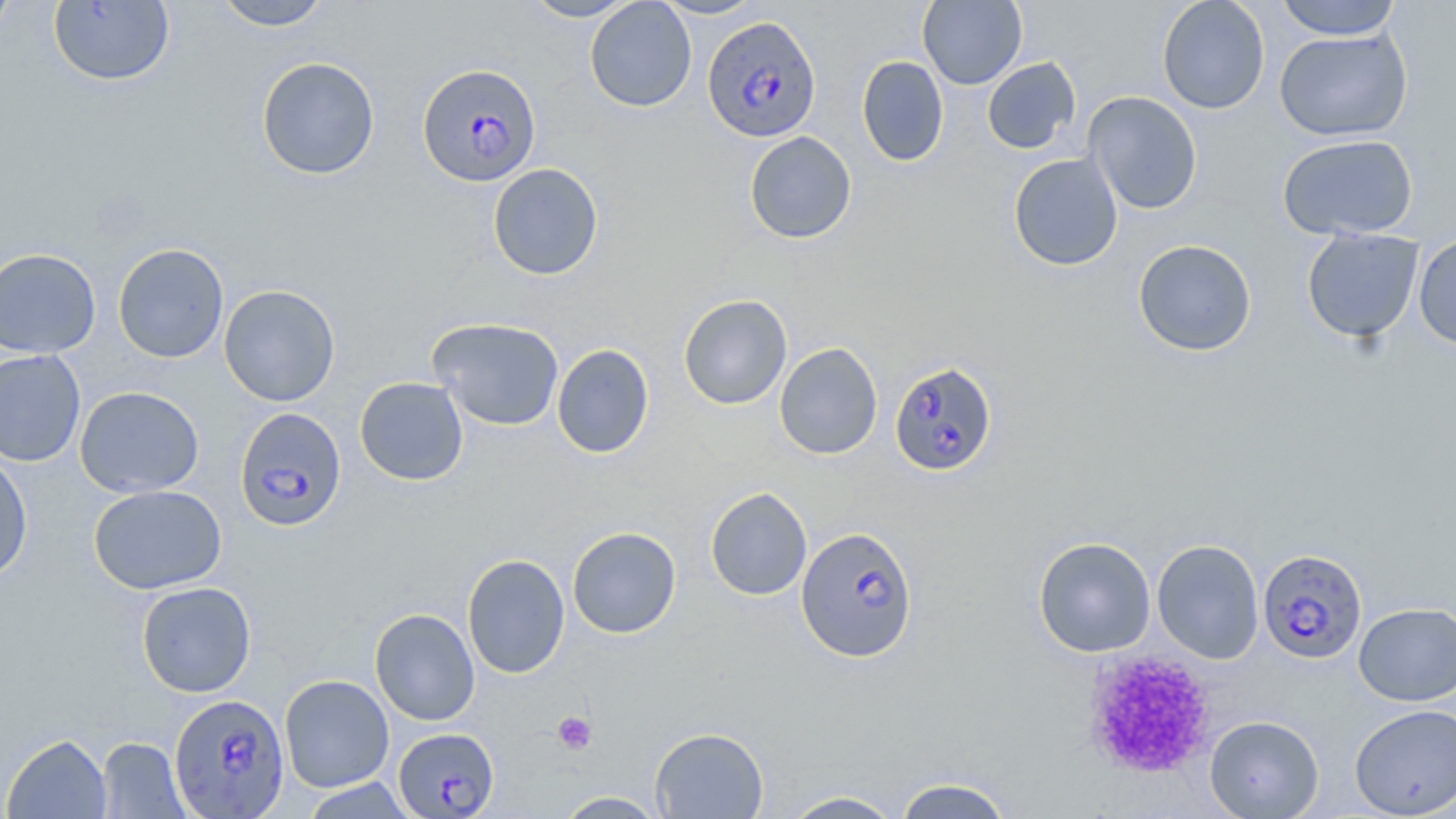
Summary:
  - Coordinate format: approximate bounding boxes as (x1,y1)-(x2,y2) corner pairs in pixels
  - Uninfected red blood cell locations: (0,0)-(17,42), (213,0)-(333,31), (521,0)-(638,21), (653,0)-(766,19), (917,0)-(1027,89), (1157,0)-(1270,114), (1274,0)-(1403,40), (48,1)-(175,87), (584,1)-(696,112), (1274,28)-(1412,142), (856,56)-(949,166), (256,57)-(380,180), (982,57)-(1081,154), (1083,91)-(1203,215), (743,131)-(857,244), (1277,134)-(1418,240), (1008,153)-(1123,271), (487,163)-(604,280), (1301,229)-(1424,343), (1413,233)-(1456,350), (1133,239)-(1257,357), (113,243)-(229,363), (0,248)-(102,359), (218,285)-(341,407), (678,294)-(792,410), (427,317)-(565,431), (774,342)-(883,460), (552,344)-(654,459), (0,349)-(86,467), (354,376)-(469,486), (75,386)-(204,498), (0,451)-(33,582), (88,485)-(227,595), (705,486)-(812,601), (567,526)-(681,638), (1032,536)-(1156,657), (1152,539)-(1264,664), (462,554)-(570,678), (136,581)-(256,697), (1354,601)-(1456,706), (370,608)-(480,725), (279,674)-(394,792), (1349,703)-(1456,818), (1204,715)-(1324,818), (650,726)-(769,818), (2,733)-(112,818), (96,737)-(190,818), (893,775)-(1016,818), (299,778)-(417,818), (781,790)-(905,818), (553,791)-(669,818)
  - Plasmodium falciparum-infected red blood cell locations: (702,15)-(821,142), (417,62)-(542,187), (889,360)-(998,475), (234,407)-(346,532), (795,525)-(919,663), (1258,548)-(1368,664), (169,694)-(291,818), (393,729)-(499,818)
  - Platelet locations: (1081,649)-(1217,779), (552,711)-(597,754)
  - Slide-level diagnosis: Plasmodium falciparum
  - Magnification: 1000x
  - Modality: light microscopy
  - Field of view: single
  - Image size: 1456×819 pixels
  - Preparation: thin blood film
  - Stain: May-Grünwald-Giemsa